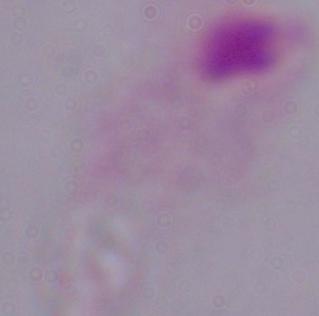
identification: trichomonad
modality: micrograph
magnification: 1000x